Locate and identify every blood parasite.
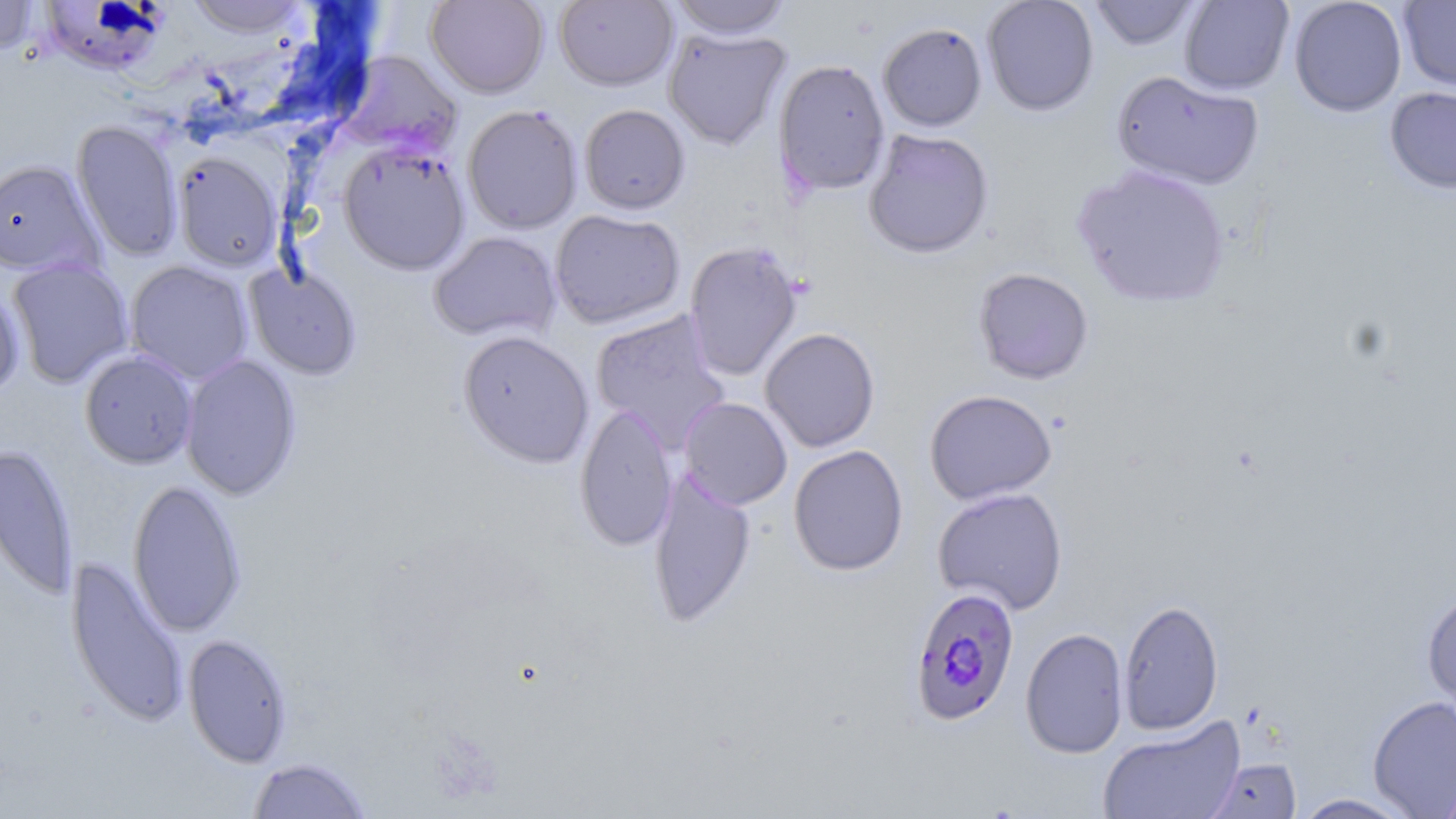

Approximate bounding boxes as named x1/y1/x2/y2 corners in pixels.
Plasmodium falciparum-infected red blood cells: (x1=908, y1=587, x2=1020, y2=726).
No Plasmodium ovale, Plasmodium malariae, Plasmodium vivax, Babesia divergens, or Trypanosoma brucei observed.

Uninfected red blood cell locations: (x1=0, y1=0, x2=42, y2=56), (x1=184, y1=0, x2=313, y2=39), (x1=425, y1=0, x2=548, y2=98), (x1=668, y1=0, x2=793, y2=40), (x1=981, y1=0, x2=1099, y2=116), (x1=1086, y1=0, x2=1202, y2=50), (x1=1178, y1=0, x2=1294, y2=96), (x1=1288, y1=0, x2=1407, y2=117), (x1=1397, y1=0, x2=1456, y2=93), (x1=554, y1=1, x2=677, y2=91), (x1=37, y1=2, x2=167, y2=75), (x1=878, y1=22, x2=987, y2=132), (x1=663, y1=26, x2=791, y2=150), (x1=336, y1=50, x2=462, y2=158), (x1=773, y1=59, x2=890, y2=196), (x1=1110, y1=71, x2=1265, y2=191), (x1=1384, y1=87, x2=1456, y2=195), (x1=462, y1=104, x2=583, y2=235), (x1=579, y1=104, x2=690, y2=215), (x1=71, y1=120, x2=184, y2=261), (x1=863, y1=129, x2=994, y2=260), (x1=338, y1=141, x2=471, y2=275), (x1=172, y1=152, x2=285, y2=272), (x1=0, y1=159, x2=104, y2=277), (x1=1071, y1=163, x2=1232, y2=309), (x1=549, y1=209, x2=685, y2=329), (x1=428, y1=231, x2=562, y2=343), (x1=683, y1=241, x2=803, y2=381), (x1=8, y1=258, x2=134, y2=388), (x1=125, y1=260, x2=254, y2=384), (x1=245, y1=262, x2=363, y2=380), (x1=973, y1=267, x2=1094, y2=385), (x1=0, y1=287, x2=25, y2=400), (x1=590, y1=309, x2=731, y2=451), (x1=760, y1=327, x2=880, y2=452), (x1=457, y1=330, x2=594, y2=468), (x1=79, y1=350, x2=198, y2=469), (x1=180, y1=354, x2=302, y2=501), (x1=924, y1=389, x2=1057, y2=505), (x1=679, y1=396, x2=793, y2=510), (x1=574, y1=402, x2=678, y2=553), (x1=0, y1=442, x2=79, y2=602), (x1=788, y1=444, x2=909, y2=576), (x1=647, y1=467, x2=757, y2=630), (x1=127, y1=479, x2=247, y2=638), (x1=932, y1=486, x2=1068, y2=614), (x1=65, y1=555, x2=189, y2=728), (x1=1421, y1=589, x2=1456, y2=719), (x1=1118, y1=599, x2=1224, y2=735), (x1=1020, y1=628, x2=1129, y2=758), (x1=183, y1=633, x2=293, y2=768), (x1=1367, y1=695, x2=1456, y2=818), (x1=1098, y1=716, x2=1246, y2=819), (x1=246, y1=757, x2=374, y2=818), (x1=1207, y1=759, x2=1302, y2=818), (x1=1436, y1=772, x2=1456, y2=819), (x1=1292, y1=793, x2=1416, y2=818). Slide-level diagnosis: Plasmodium falciparum. Image is 1456×819 pixels. May-Grünwald-Giemsa stain. Optical microscopy. Single field of view. Thin blood film. Captured at 1000x magnification.